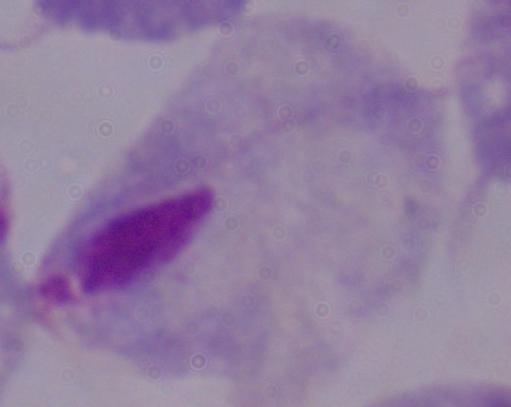

{
  "identification": "trichomonad",
  "magnification": "1000x",
  "modality": "micrograph"
}